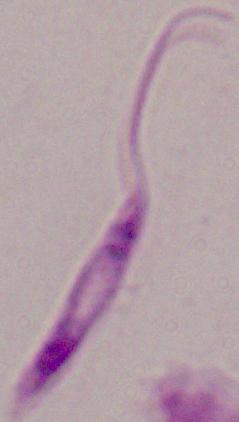
{
  "magnification": "1000x",
  "identification": "Leishmania",
  "modality": "photomicrograph"
}